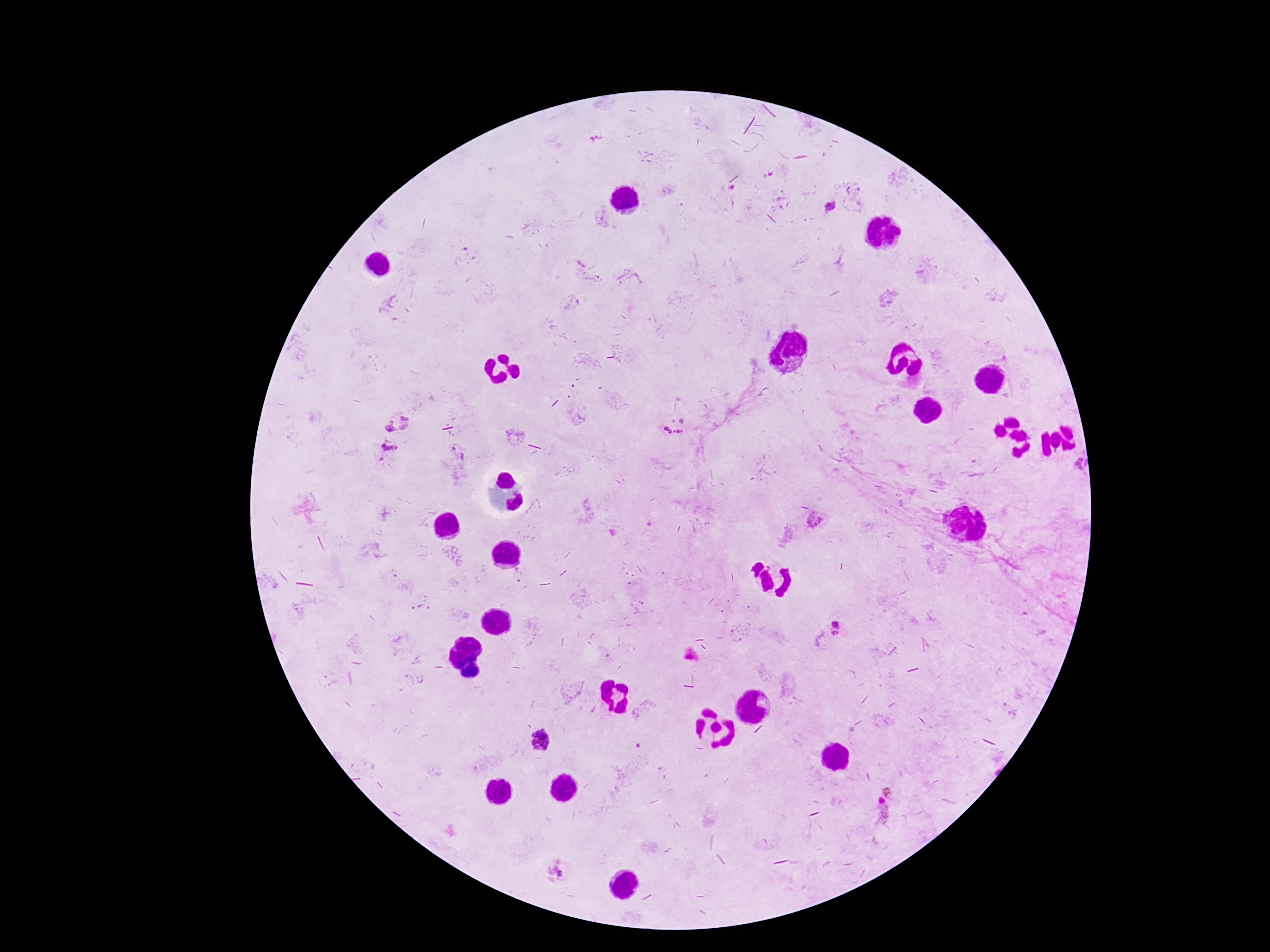
Approximate centers as (x, y) in pixels. Plasmodium parasite locations: (831, 207), (682, 422), (397, 423), (667, 430), (674, 431), (678, 431), (682, 431), (390, 450), (463, 456), (381, 459), (814, 520), (516, 569), (519, 581), (837, 624), (836, 634), (542, 740), (887, 792), (880, 801), (556, 871). Smartphone photograph taken through the microscope eyepiece. Giemsa-stained preparation. Image is 1270×952 pixels. 100x magnification. Patient malaria status: infected. One field from this slide. Thick peripheral-blood smear.